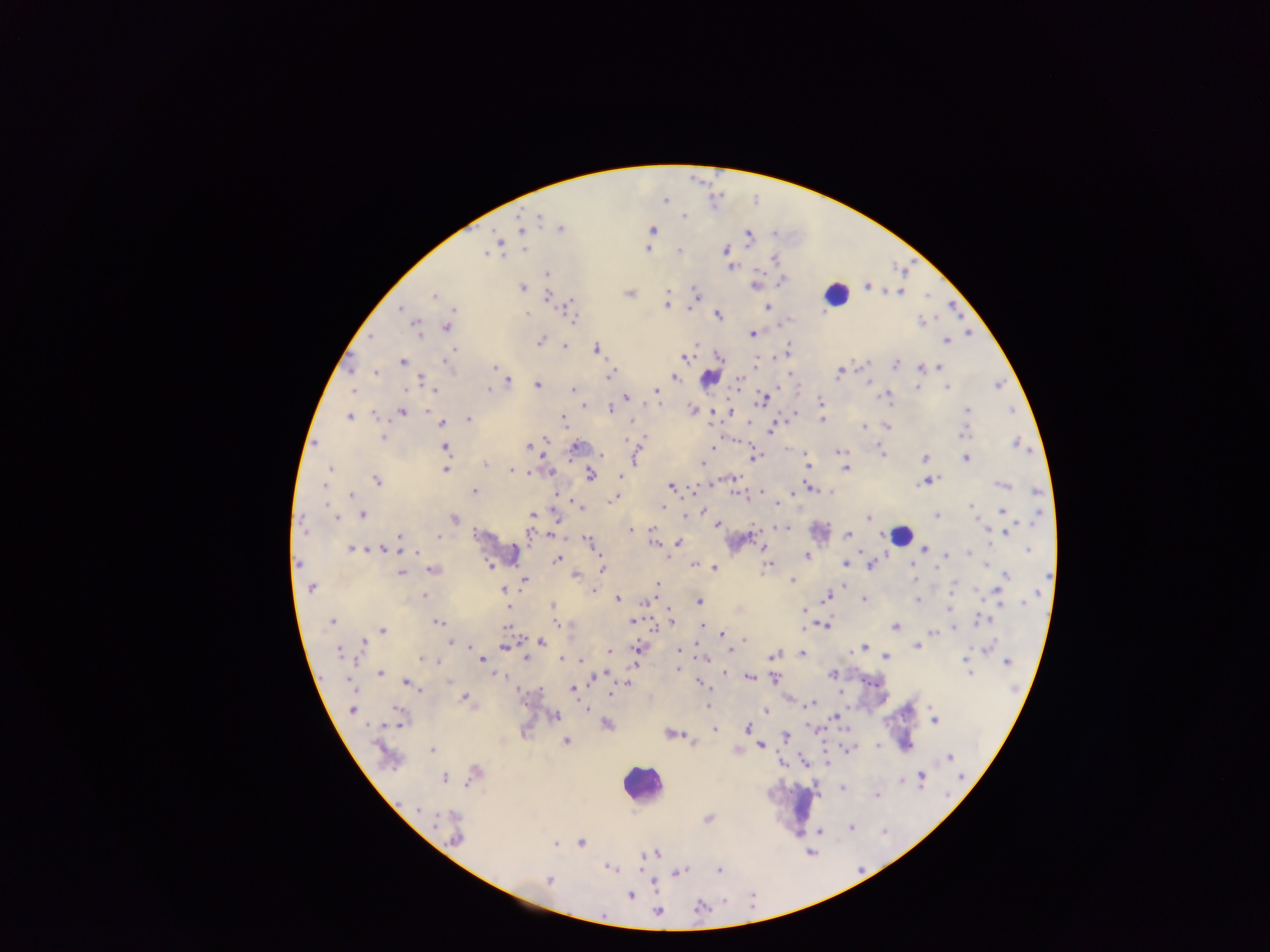
{
  "image_size": "1270×952 pixels",
  "country": "Ghana",
  "field_of_view": "single",
  "preparation": "thick blood smear",
  "leukocyte_locations": "approximate centers as {x, y} in pixels: {835, 294}, {899, 535}, {640, 784}, {803, 803}",
  "capture": "mobile-phone photograph through a microscope",
  "plasmodium_parasite_locations": "approximate centers as {x, y} in pixels: {665, 200}, {684, 216}, {538, 217}, {561, 228}, {522, 229}, {652, 230}, {775, 234}, {748, 238}, {524, 250}, {647, 250}, {725, 250}, {679, 252}, {486, 253}, {775, 259}, {732, 267}, {546, 274}, {782, 280}, {755, 286}, {867, 287}, {522, 288}, {901, 292}, {629, 293}, {696, 293}, {434, 296}, {547, 296}, {667, 305}, {767, 307}, {569, 308}, {400, 309}, {719, 316}, {572, 319}, {921, 322}, {447, 327}, {416, 330}, {753, 333}, {371, 338}, {541, 341}, {946, 341}, {564, 347}, {788, 349}, {597, 350}, {685, 357}, {720, 357}, {402, 361}, {756, 361}, {449, 364}, {867, 364}, {896, 365}, {493, 367}, {941, 367}, {920, 368}, {374, 374}, {839, 374}, {610, 375}, {675, 377}, {708, 378}, {422, 380}, {738, 381}, {509, 382}, {869, 382}, {537, 385}, {999, 385}, {917, 387}, {947, 388}, {407, 389}, {488, 389}, {573, 389}, {353, 390}, {433, 390}, {656, 390}, {888, 395}, {625, 397}, {763, 400}, {821, 401}, {584, 405}, {610, 409}, {692, 409}, {967, 410}, {1012, 410}, {402, 412}, {731, 412}, {794, 414}, {375, 415}, {349, 417}, {468, 419}, {564, 420}, {822, 420}, {632, 422}, {441, 423}, {750, 424}, {887, 426}, {863, 427}, {772, 429}, {964, 433}, {383, 437}, {544, 440}, {1016, 443}, {528, 445}, {445, 447}, {576, 447}, {712, 448}, {838, 451}, {601, 454}, {882, 454}, {755, 457}, {635, 458}, {924, 459}, {965, 459}, {485, 463}, {702, 464}, {807, 465}, {330, 468}, {845, 468}, {445, 469}, {512, 472}, {550, 472}, {530, 473}, {591, 475}, {621, 477}, {377, 480}, {929, 480}, {924, 482}, {323, 485}, {1001, 485}, {670, 486}, {810, 488}, {761, 490}, {474, 491}, {1037, 492}, {352, 494}, {737, 494}, {559, 496}, {614, 499}, {777, 503}, {579, 506}, {972, 507}, {663, 508}, {1003, 509}, {702, 511}, {363, 515}, {532, 515}, {937, 515}, {336, 516}, {685, 516}, {867, 517}, {1039, 517}, {454, 518}, {556, 519}, {717, 525}, {784, 529}, {630, 530}, {1007, 532}, {530, 533}, {552, 535}, {848, 535}, {399, 537}, {439, 537}, {589, 542}, {679, 542}, {654, 543}, {351, 548}, {382, 549}, {924, 549}, {764, 550}, {1027, 550}, {416, 552}, {861, 552}, {946, 555}, {806, 556}, {557, 559}, {298, 563}, {845, 563}, {695, 564}, {911, 565}, {987, 565}, {767, 566}, {870, 566}, {715, 568}, {603, 569}, {432, 570}, {401, 574}, {575, 575}, {1007, 575}, {1046, 577}, {915, 579}, {524, 580}, {792, 580}, {656, 585}, {953, 586}, {310, 588}, {503, 589}, {592, 590}, {423, 596}, {826, 596}, {998, 596}, {1036, 596}, {618, 599}, {649, 600}, {918, 600}, {864, 601}, {699, 602}, {1025, 602}, {1000, 604}, {552, 605}, {508, 608}, {949, 608}, {553, 610}, {804, 610}, {671, 620}, {981, 620}, {332, 621}, {632, 622}, {438, 623}, {555, 623}, {667, 624}, {702, 625}, {827, 625}, {505, 627}, {894, 627}, {954, 628}, {382, 630}, {932, 632}, {722, 635}, {744, 640}, {541, 642}, {364, 643}, {451, 643}, {468, 647}, {504, 647}, {917, 647}, {864, 648}, {989, 648}, {638, 649}, {731, 650}, {859, 650}, {471, 651}, {610, 651}, {679, 651}, {851, 651}, {339, 652}, {803, 654}, {774, 655}, {886, 656}, {422, 658}, {526, 658}, {705, 658}, {482, 659}, {561, 659}, {581, 660}, {965, 661}, {1006, 662}, {677, 668}, {967, 668}, {726, 673}, {970, 673}, {380, 674}, {832, 674}, {604, 675}, {500, 676}, {594, 677}, {748, 677}, {775, 679}, {448, 682}, {407, 683}, {701, 683}, {351, 685}, {628, 685}, {573, 689}, {611, 693}, {840, 693}, {465, 698}, {810, 704}, {708, 705}, {586, 709}, {352, 710}, {396, 710}, {766, 711}, {556, 716}, {835, 717}, {399, 720}, {934, 720}, {606, 724}, {747, 728}, {715, 729}, {670, 734}, {786, 737}, {694, 741}, {566, 742}, {761, 745}, {876, 745}, {850, 748}, {432, 750}, {950, 758}, {827, 763}, {476, 773}, {921, 776}, {961, 777}, {445, 779}, {842, 788}, {876, 795}, {418, 809}, {708, 819}, {435, 822}, {852, 827}, {456, 839}, {581, 843}, {556, 844}, {650, 854}, {610, 869}, {720, 871}, {678, 873}, {548, 880}, {630, 896}, {701, 906}, {657, 912}"
}